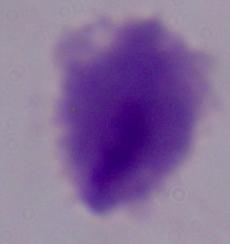
1000x magnification. A trichomonad is seen. Micrograph.